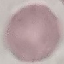
result = negative for malaria parasites
image type = automatically extracted cell patch, resized to 64 × 64 pixels
preparation = thin blood film
capture = smartphone through the microscope eyepiece
stain = Giemsa